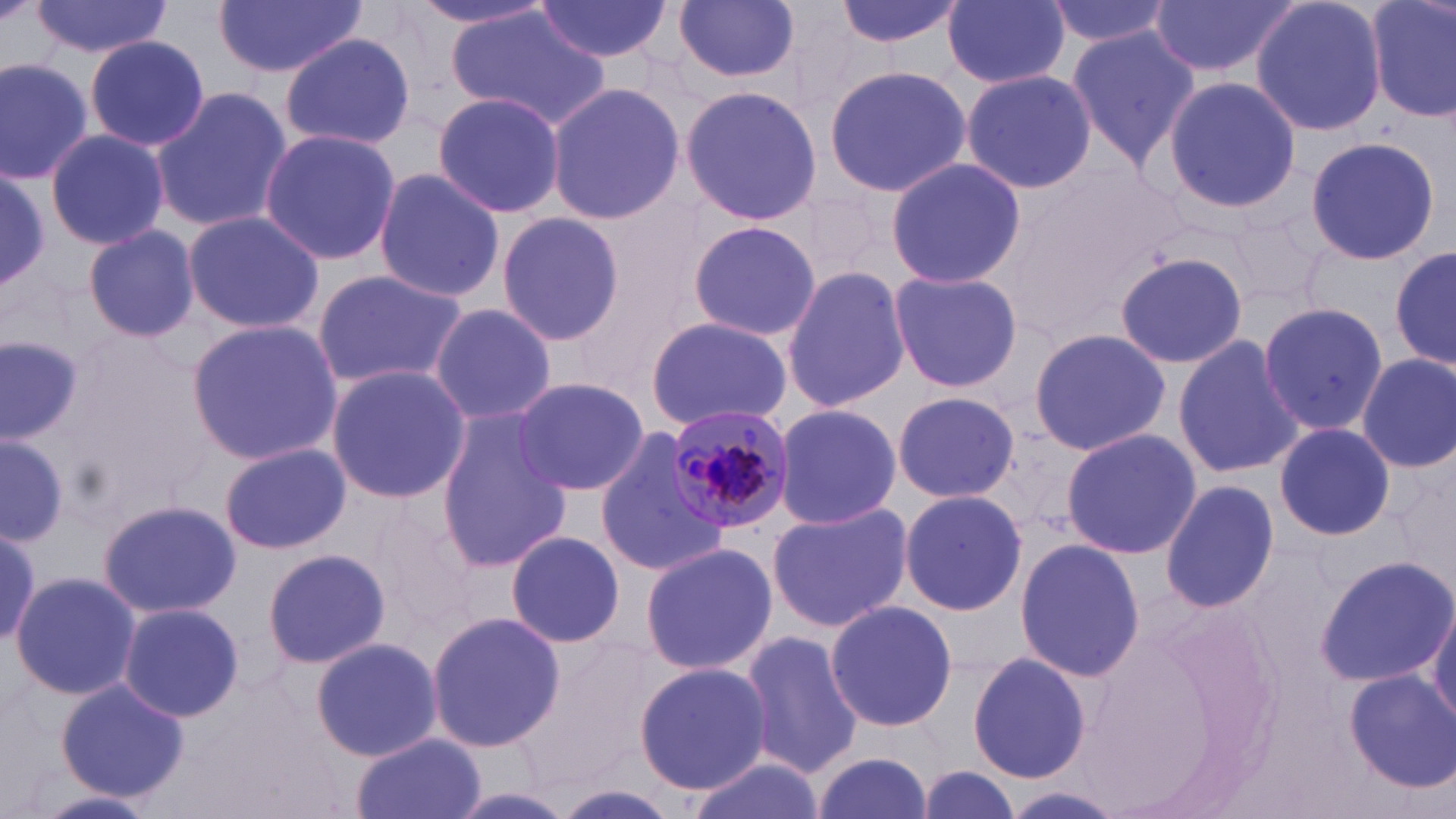

Summary:
  - Coordinate format: approximate bounding boxes as [x1, y1, x2, y2] in pixels
  - Uninfected red blood cell locations: [32, 0, 172, 58], [216, 0, 366, 79], [406, 0, 558, 34], [533, 0, 672, 64], [674, 0, 801, 85], [834, 0, 963, 51], [944, 0, 1070, 89], [1045, 0, 1176, 49], [1149, 0, 1299, 81], [1249, 0, 1388, 139], [1366, 0, 1455, 126], [450, 8, 609, 130], [1066, 28, 1199, 171], [280, 33, 415, 152], [83, 35, 211, 153], [0, 55, 94, 181], [824, 63, 971, 199], [960, 69, 1097, 195], [1161, 76, 1304, 214], [546, 84, 687, 227], [680, 85, 821, 226], [151, 86, 292, 234], [433, 92, 564, 218], [42, 128, 169, 250], [258, 128, 403, 266], [1303, 133, 1443, 268], [883, 157, 1027, 287], [371, 168, 506, 305], [0, 170, 51, 288], [183, 210, 325, 333], [495, 210, 624, 346], [1224, 212, 1332, 310], [686, 219, 820, 343], [83, 225, 200, 343], [1391, 244, 1456, 372], [1113, 250, 1249, 371], [781, 265, 910, 413], [313, 270, 467, 391], [886, 270, 1023, 392], [1258, 300, 1389, 434], [429, 302, 556, 424], [647, 316, 792, 430], [185, 320, 341, 464], [1027, 328, 1170, 458], [0, 333, 87, 442], [1172, 335, 1305, 478], [1356, 353, 1456, 472], [326, 366, 471, 503], [508, 376, 649, 498], [892, 391, 1020, 502], [773, 403, 902, 531], [436, 414, 572, 574], [1274, 422, 1394, 541], [1061, 427, 1202, 559], [594, 429, 727, 572], [0, 434, 68, 547], [1, 435, 67, 543], [218, 442, 350, 556], [1160, 480, 1279, 613], [899, 490, 1027, 614], [98, 497, 240, 618], [767, 502, 913, 632], [0, 527, 44, 649], [505, 531, 628, 648], [1013, 539, 1146, 683], [640, 542, 775, 677], [262, 547, 391, 670], [1316, 556, 1455, 685], [11, 570, 141, 701], [826, 599, 956, 733], [1428, 599, 1456, 732], [114, 603, 246, 722], [425, 613, 563, 755], [741, 631, 863, 775], [310, 637, 443, 760], [966, 650, 1094, 785], [634, 662, 771, 794], [1341, 668, 1456, 792], [56, 679, 189, 800], [351, 733, 484, 819], [810, 751, 937, 819], [682, 754, 817, 819], [914, 765, 1023, 819], [544, 785, 684, 819], [443, 788, 579, 819], [1004, 789, 1126, 818], [39, 791, 158, 817]
  - Plasmodium malariae-infected red blood cell locations: [668, 405, 795, 535]
  - Slide-level diagnosis: Plasmodium malariae
  - Magnification: 1000x
  - Image size: 1456×819 pixels
  - Field of view: one of a larger specimen
  - Preparation: thin blood film
  - Modality: light microscopy
  - Stain: May-Grünwald-Giemsa